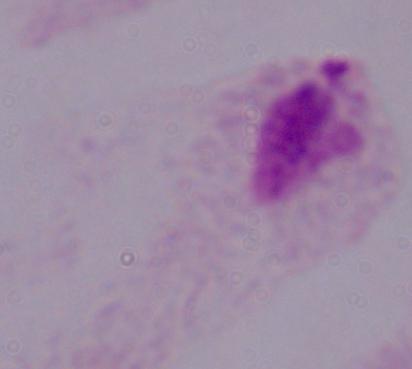

Summary:
  - Identification: trichomonad
  - Modality: photomicrograph
  - Magnification: 1000x